Locate every blood parasite and identify its species.
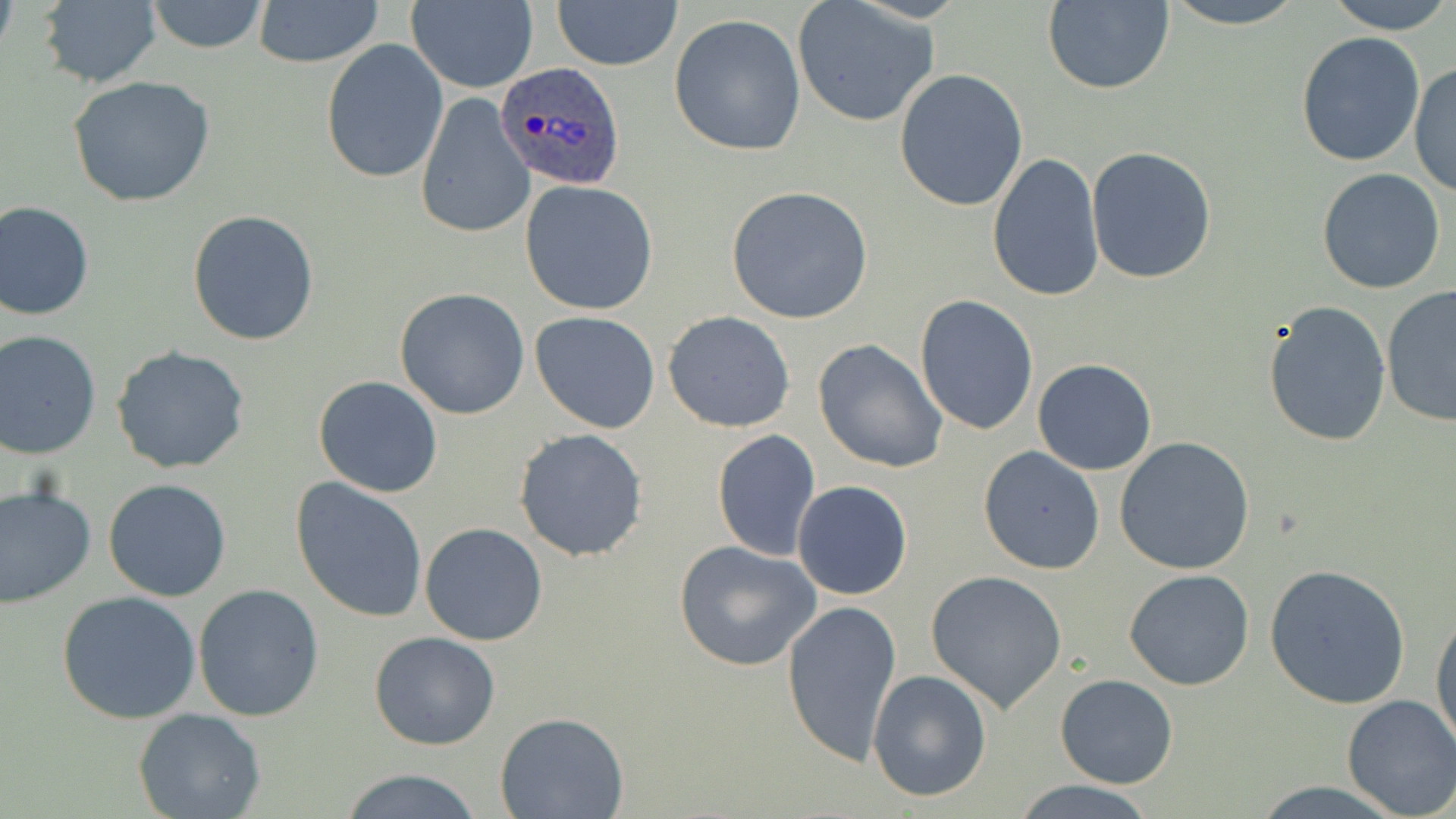

Approximate bounding boxes as named x1/y1/x2/y2 corners in pixels.
Plasmodium ovale-infected red blood cells: (x1=496, y1=62, x2=625, y2=189).
No Plasmodium falciparum, Plasmodium malariae, Plasmodium vivax, Babesia divergens, or Trypanosoma brucei observed.

{
  "slide_level_diagnosis": "Plasmodium ovale",
  "modality": "optical microscopy",
  "preparation": "thin blood film",
  "field_of_view": "one of a larger specimen",
  "stain": "May-Grünwald-Giemsa",
  "magnification": "1000x",
  "image_size": "1456×819 pixels",
  "uninfected_red_blood_cell_locations": "approximate bounding boxes as named x1/y1/x2/y2 corners in pixels: (x1=37, y1=0, x2=162, y2=88), (x1=144, y1=0, x2=271, y2=54), (x1=550, y1=0, x2=683, y2=70), (x1=1155, y1=0, x2=1313, y2=27), (x1=1321, y1=0, x2=1455, y2=35), (x1=252, y1=1, x2=383, y2=69), (x1=406, y1=1, x2=537, y2=93), (x1=1041, y1=1, x2=1176, y2=94), (x1=791, y1=2, x2=939, y2=129), (x1=667, y1=15, x2=808, y2=157), (x1=1295, y1=32, x2=1425, y2=167), (x1=321, y1=39, x2=449, y2=184), (x1=1411, y1=62, x2=1454, y2=198), (x1=894, y1=69, x2=1028, y2=213), (x1=68, y1=76, x2=217, y2=210), (x1=414, y1=93, x2=534, y2=240), (x1=1087, y1=147, x2=1218, y2=285), (x1=988, y1=153, x2=1104, y2=304), (x1=1316, y1=167, x2=1447, y2=295), (x1=519, y1=181, x2=660, y2=315), (x1=727, y1=186, x2=876, y2=325), (x1=1, y1=201, x2=95, y2=320), (x1=187, y1=208, x2=320, y2=346), (x1=1380, y1=285, x2=1456, y2=427), (x1=393, y1=288, x2=529, y2=420), (x1=914, y1=294, x2=1039, y2=436), (x1=1263, y1=300, x2=1392, y2=447), (x1=529, y1=311, x2=660, y2=433), (x1=663, y1=311, x2=795, y2=432), (x1=1, y1=330, x2=102, y2=459), (x1=812, y1=339, x2=948, y2=473), (x1=112, y1=345, x2=250, y2=474), (x1=1032, y1=358, x2=1159, y2=475), (x1=314, y1=376, x2=442, y2=498), (x1=514, y1=428, x2=650, y2=562), (x1=712, y1=429, x2=820, y2=562), (x1=1116, y1=437, x2=1257, y2=576), (x1=977, y1=445, x2=1106, y2=574), (x1=289, y1=477, x2=428, y2=621), (x1=102, y1=479, x2=232, y2=602), (x1=792, y1=481, x2=913, y2=600), (x1=0, y1=485, x2=96, y2=607), (x1=420, y1=523, x2=547, y2=645), (x1=674, y1=541, x2=822, y2=671), (x1=1263, y1=563, x2=1412, y2=710), (x1=1123, y1=569, x2=1256, y2=691), (x1=925, y1=570, x2=1067, y2=712), (x1=193, y1=585, x2=326, y2=722), (x1=58, y1=591, x2=203, y2=725), (x1=781, y1=597, x2=902, y2=768), (x1=1430, y1=607, x2=1455, y2=757), (x1=369, y1=632, x2=500, y2=750), (x1=867, y1=670, x2=992, y2=802), (x1=1055, y1=673, x2=1178, y2=789), (x1=1342, y1=694, x2=1456, y2=818), (x1=136, y1=709, x2=265, y2=819), (x1=497, y1=713, x2=628, y2=819), (x1=335, y1=770, x2=486, y2=819), (x1=1008, y1=778, x2=1157, y2=817)"
}